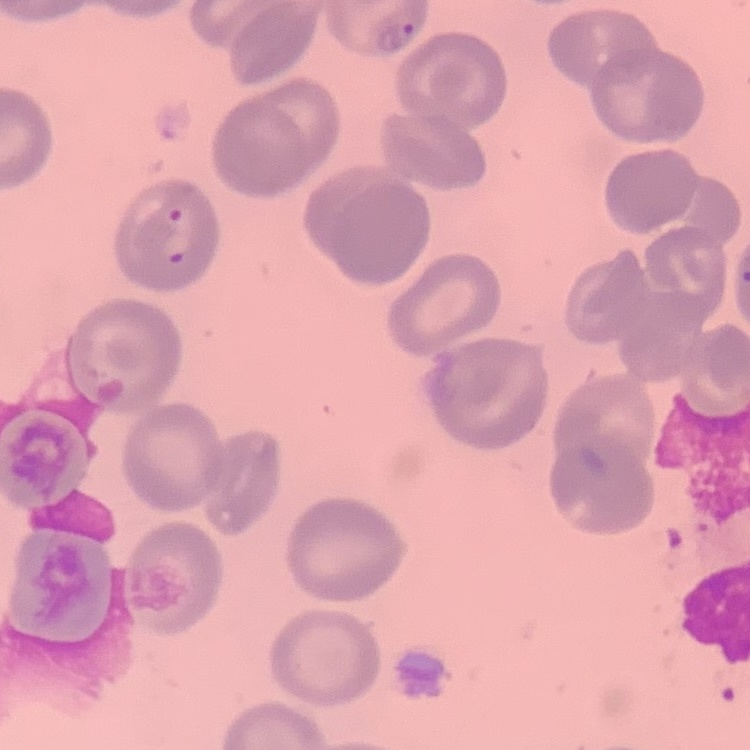

Summary:
  - Red blood cell morphology: no rouleaux formation
  - Stain: Field's or Giemsa
  - Preparation: thin blood smear
  - Image type: one tile cut from a larger photomicrograph